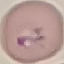
Summary:
  - Result: malaria parasites identified
  - Image type: cell patch, automatically extracted from a larger field of view and resized to 64 × 64 pixels
  - Capture: smartphone camera at the microscope eyepiece
  - Preparation: thin blood film
  - Stain: Giemsa